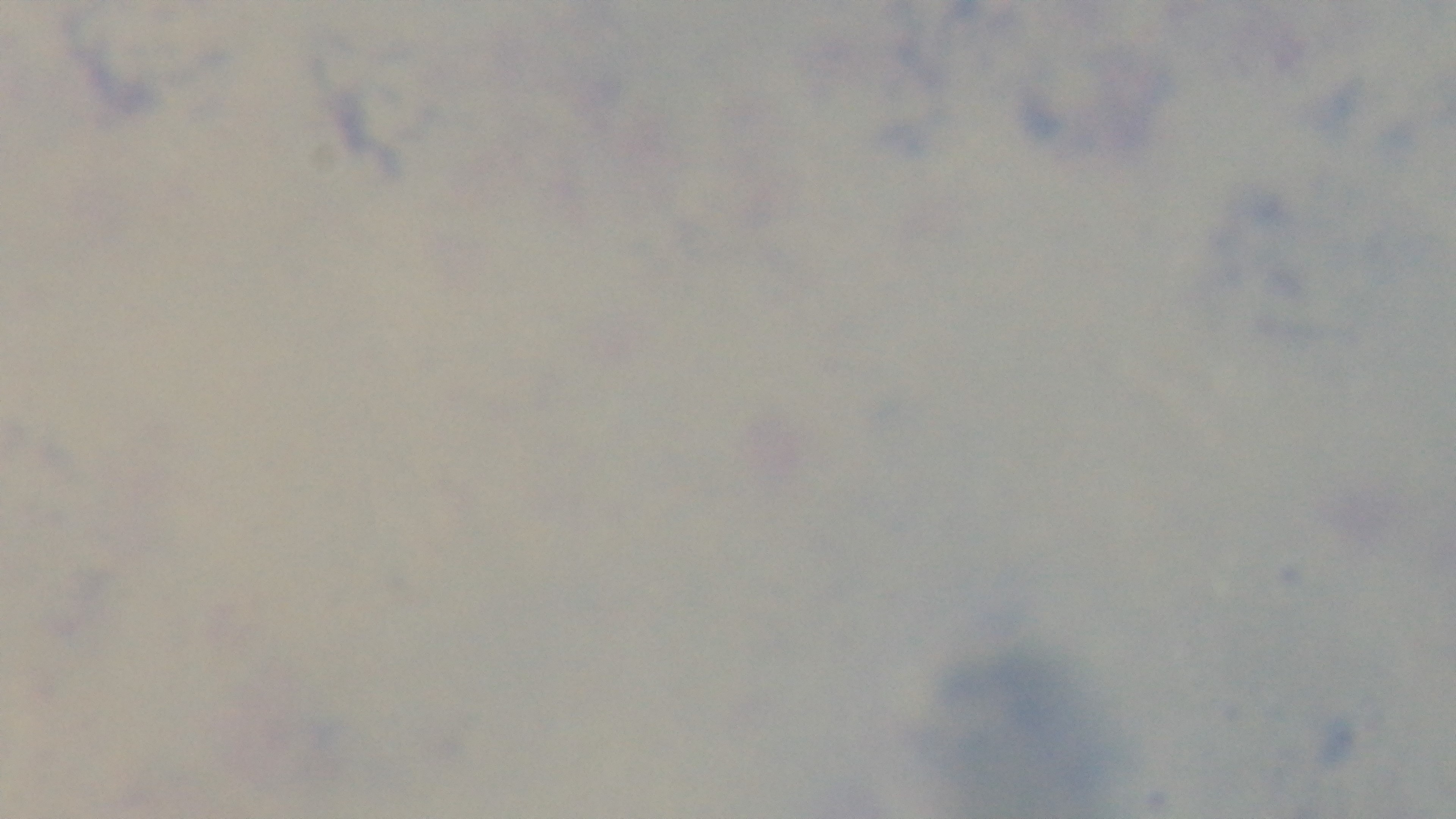
capture = mounted 4K digital camera
objective = 100x oil immersion
field of view = one from the slide
preparation = thick
malaria status = negative
stain = Giemsa
modality = light microscopy